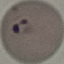
Result: malaria parasites detected. Photographed with a smartphone camera at the microscope eyepiece. Automatically extracted cell patch, resized to 64 × 64 pixels. Thin blood smear. Giemsa-stained preparation.